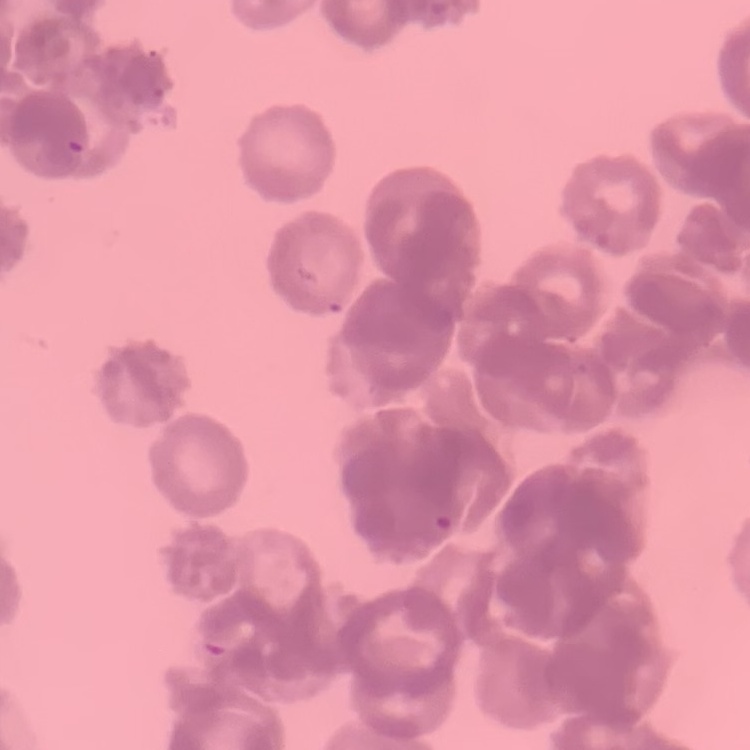
Summary:
  - Red blood cell morphology: rouleaux formation
  - Preparation: thin blood film
  - Stain: Field's or Giemsa
  - Image type: one tile cut from a larger photomicrograph